Assess the morphology of the erythrocytes.
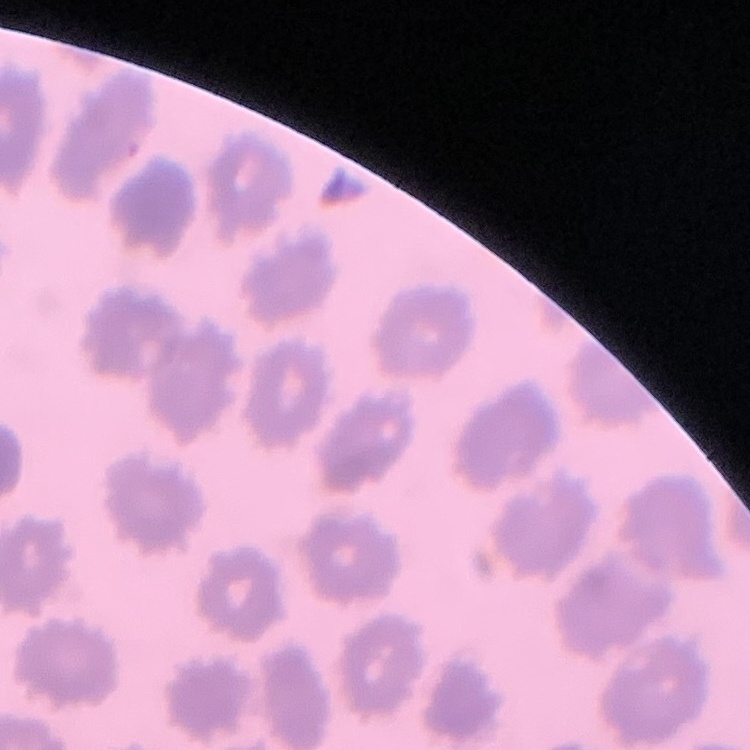
They show no rouleaux formation.

image type = one tile cut from a larger photomicrograph
stain = Field's or Giemsa
preparation = thin blood film